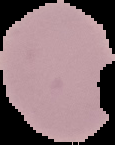
malaria_status: uninfected
preparation: thin blood film
image_type: cell region segmented out of the field of view; surrounding area masked to black
image_size: 115×145 pixels